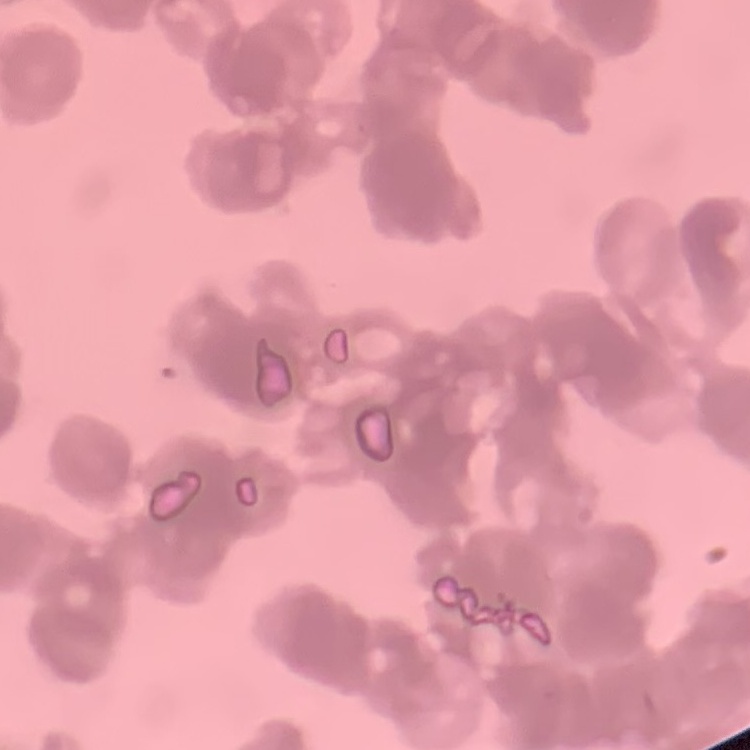
Summary:
  - Red blood cell morphology: rouleaux formation
  - Stain: Field's or Giemsa
  - Image type: square crop of a larger photomicrograph
  - Preparation: thin blood smear